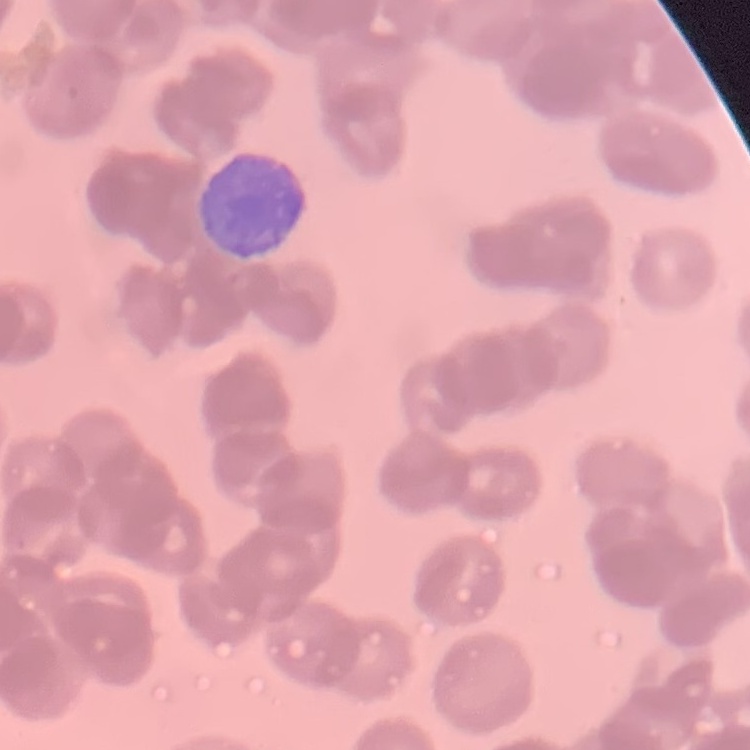 The red blood cells exhibit rouleaux formation. One tile cut from a larger photomicrograph. Thin blood smear. Stained with either Field's or Giemsa.